Name the parasite shown.
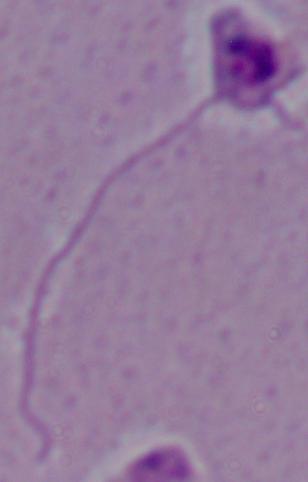
Leishmania.

Captured at 1000x magnification. Photomicrograph.